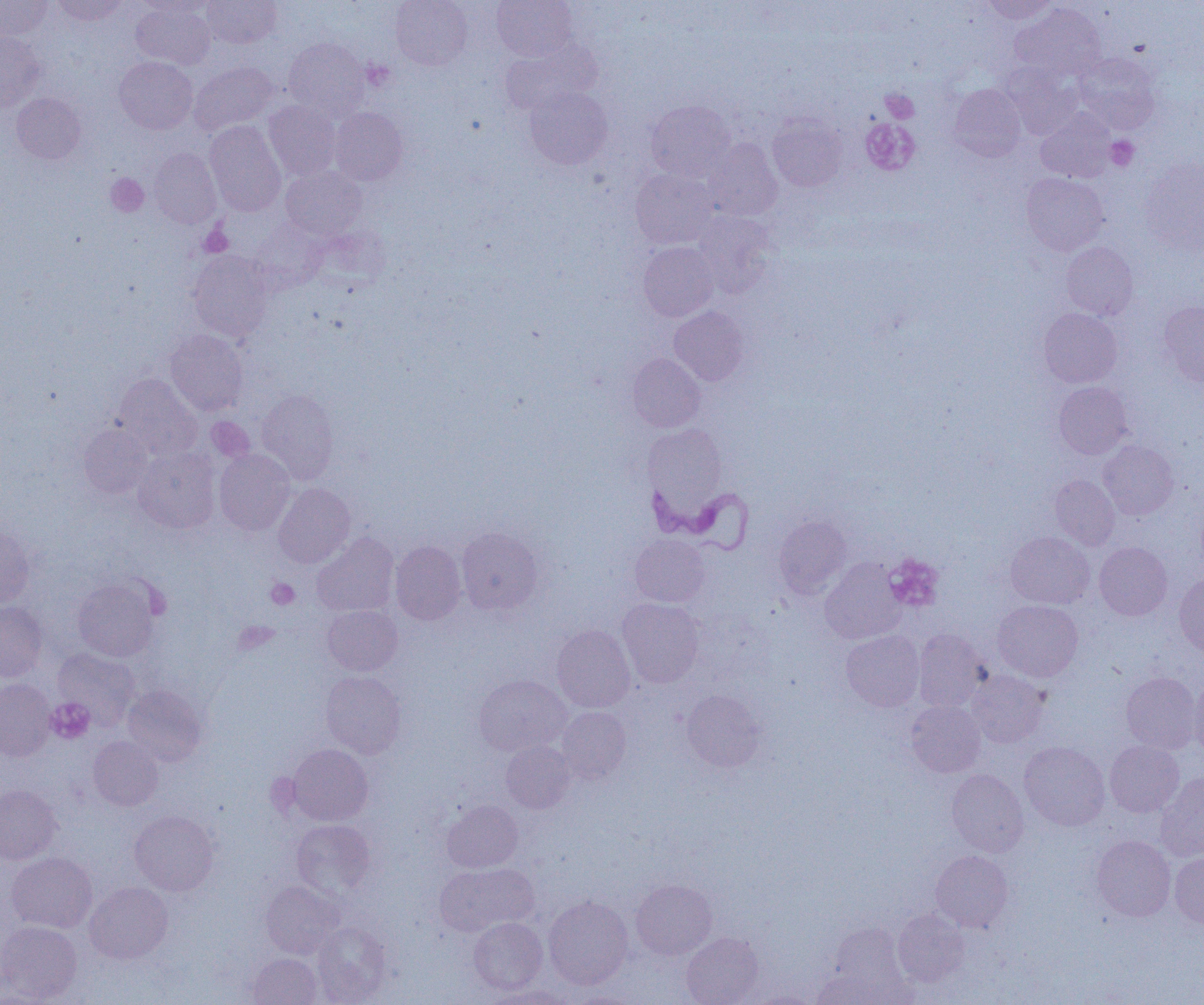 Approximate bounding boxes as named x1/y1/x2/y2 corners in pixels. Trypanosoma brucei locations: (x1=644, y1=475, x2=754, y2=554). Uninfected red blood cell locations (subset): (x1=0, y1=0, x2=51, y2=40), (x1=51, y1=0, x2=128, y2=26), (x1=132, y1=0, x2=213, y2=17), (x1=202, y1=0, x2=281, y2=48), (x1=391, y1=0, x2=472, y2=70), (x1=492, y1=0, x2=578, y2=61), (x1=980, y1=0, x2=1059, y2=24), (x1=131, y1=2, x2=215, y2=68), (x1=1011, y1=3, x2=1107, y2=82), (x1=0, y1=32, x2=45, y2=112), (x1=284, y1=38, x2=369, y2=119), (x1=499, y1=40, x2=600, y2=116), (x1=1074, y1=53, x2=1161, y2=133), (x1=114, y1=56, x2=198, y2=134), (x1=189, y1=62, x2=278, y2=135), (x1=1002, y1=66, x2=1081, y2=139), (x1=948, y1=84, x2=1026, y2=161), (x1=524, y1=86, x2=612, y2=169), (x1=11, y1=93, x2=86, y2=164), (x1=264, y1=101, x2=340, y2=180), (x1=645, y1=101, x2=735, y2=181), (x1=330, y1=107, x2=407, y2=185), (x1=1036, y1=109, x2=1115, y2=182), (x1=767, y1=114, x2=847, y2=192), (x1=204, y1=120, x2=286, y2=216), (x1=703, y1=139, x2=782, y2=220), (x1=149, y1=148, x2=221, y2=228), (x1=1140, y1=158, x2=1204, y2=253), (x1=281, y1=166, x2=366, y2=240), (x1=630, y1=168, x2=718, y2=248), (x1=1021, y1=172, x2=1109, y2=255), (x1=692, y1=212, x2=775, y2=296), (x1=638, y1=242, x2=718, y2=321), (x1=1061, y1=242, x2=1138, y2=321), (x1=188, y1=251, x2=273, y2=341), (x1=1159, y1=301, x2=1204, y2=387), (x1=669, y1=306, x2=749, y2=386), (x1=1039, y1=308, x2=1122, y2=388), (x1=164, y1=329, x2=248, y2=415), (x1=627, y1=353, x2=705, y2=432), (x1=113, y1=374, x2=202, y2=460), (x1=1053, y1=382, x2=1132, y2=459), (x1=257, y1=389, x2=339, y2=484), (x1=79, y1=425, x2=153, y2=498), (x1=644, y1=425, x2=726, y2=510), (x1=1098, y1=441, x2=1178, y2=519), (x1=133, y1=447, x2=220, y2=533), (x1=214, y1=449, x2=295, y2=535), (x1=1050, y1=475, x2=1119, y2=550), (x1=273, y1=482, x2=355, y2=568), (x1=773, y1=515, x2=852, y2=598), (x1=0, y1=523, x2=35, y2=608), (x1=456, y1=527, x2=543, y2=615), (x1=1005, y1=531, x2=1094, y2=608), (x1=312, y1=533, x2=399, y2=616), (x1=630, y1=534, x2=710, y2=607), (x1=391, y1=541, x2=465, y2=624), (x1=1094, y1=542, x2=1172, y2=620), (x1=820, y1=559, x2=907, y2=644), (x1=1175, y1=573, x2=1204, y2=656), (x1=72, y1=578, x2=159, y2=661), (x1=617, y1=598, x2=704, y2=687), (x1=992, y1=600, x2=1083, y2=682), (x1=0, y1=601, x2=48, y2=682), (x1=323, y1=605, x2=402, y2=675), (x1=552, y1=625, x2=635, y2=712), (x1=913, y1=629, x2=990, y2=711), (x1=841, y1=630, x2=924, y2=711), (x1=53, y1=648, x2=140, y2=729), (x1=966, y1=670, x2=1048, y2=748), (x1=320, y1=671, x2=406, y2=758), (x1=1121, y1=672, x2=1202, y2=754), (x1=474, y1=674, x2=571, y2=756), (x1=1189, y1=676, x2=1204, y2=759), (x1=0, y1=679, x2=55, y2=760), (x1=122, y1=684, x2=208, y2=766), (x1=682, y1=689, x2=766, y2=772), (x1=906, y1=701, x2=986, y2=777), (x1=557, y1=707, x2=631, y2=783), (x1=88, y1=737, x2=163, y2=810), (x1=1105, y1=740, x2=1184, y2=817), (x1=501, y1=741, x2=575, y2=813), (x1=1019, y1=741, x2=1110, y2=831), (x1=287, y1=744, x2=373, y2=825), (x1=946, y1=770, x2=1028, y2=856), (x1=1156, y1=772, x2=1204, y2=861), (x1=0, y1=785, x2=61, y2=864), (x1=442, y1=800, x2=522, y2=872), (x1=129, y1=810, x2=219, y2=895), (x1=291, y1=819, x2=375, y2=896), (x1=1091, y1=835, x2=1175, y2=921), (x1=931, y1=850, x2=1013, y2=931), (x1=7, y1=853, x2=97, y2=933), (x1=1170, y1=853, x2=1204, y2=928), (x1=434, y1=863, x2=538, y2=935), (x1=631, y1=879, x2=717, y2=959), (x1=261, y1=881, x2=343, y2=959), (x1=85, y1=882, x2=173, y2=964), (x1=544, y1=895, x2=633, y2=989), (x1=893, y1=909, x2=968, y2=986), (x1=469, y1=917, x2=547, y2=994), (x1=0, y1=921, x2=82, y2=1002), (x1=313, y1=921, x2=392, y2=1003), (x1=826, y1=922, x2=910, y2=998), (x1=681, y1=932, x2=764, y2=1005), (x1=246, y1=943, x2=391, y2=1004), (x1=247, y1=953, x2=322, y2=1005), (x1=1, y1=965, x2=45, y2=1005), (x1=810, y1=970, x2=890, y2=1005), (x1=483, y1=985, x2=574, y2=1004), (x1=568, y1=991, x2=642, y2=1004). Platelet locations (subset): (x1=361, y1=60, x2=395, y2=91), (x1=882, y1=89, x2=919, y2=122), (x1=1106, y1=136, x2=1139, y2=171), (x1=105, y1=173, x2=149, y2=217), (x1=200, y1=225, x2=233, y2=257), (x1=206, y1=418, x2=254, y2=462), (x1=885, y1=554, x2=944, y2=612), (x1=267, y1=578, x2=300, y2=609), (x1=234, y1=622, x2=277, y2=654), (x1=46, y1=698, x2=94, y2=743). Slide-level diagnosis: Trypanosoma brucei. Light microscopy. Single field of view. Image is 1204×1005 pixels. Thin blood film. Captured at 1000x magnification.